Report the malaria status of this cell.
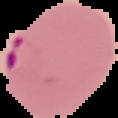

It is parasitized.

image size = 118×118 pixels
preparation = thin blood smear
image type = cell region segmented out of the field of view; surrounding area masked to black